Assess this cell for malaria.
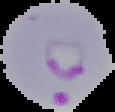
It is parasitized.

image type = segmented cell region on a black background
preparation = thin blood film
image size = 115×112 pixels